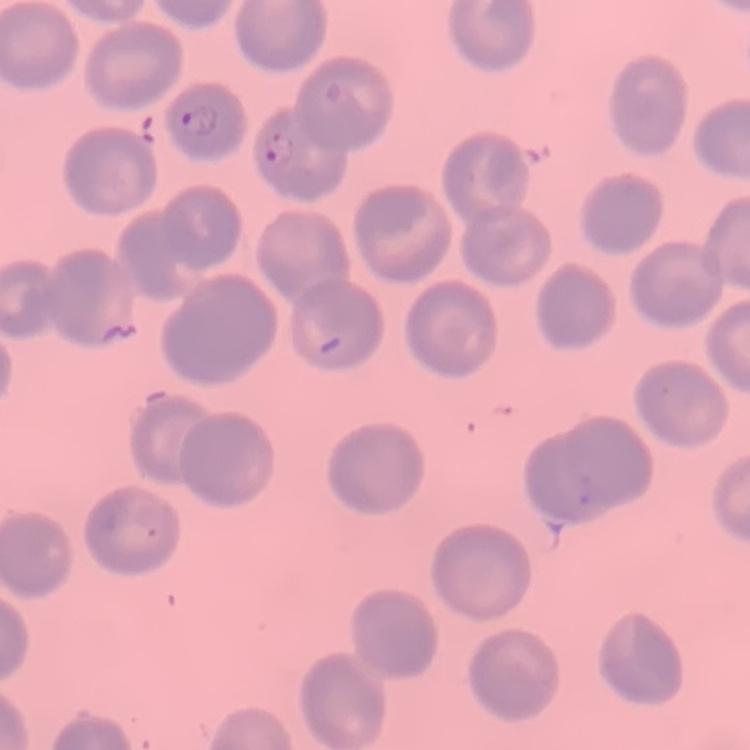 The erythrocytes show no rouleaux formation. One tile cut from a larger photomicrograph. Field's or Giemsa stain. Thin blood film.